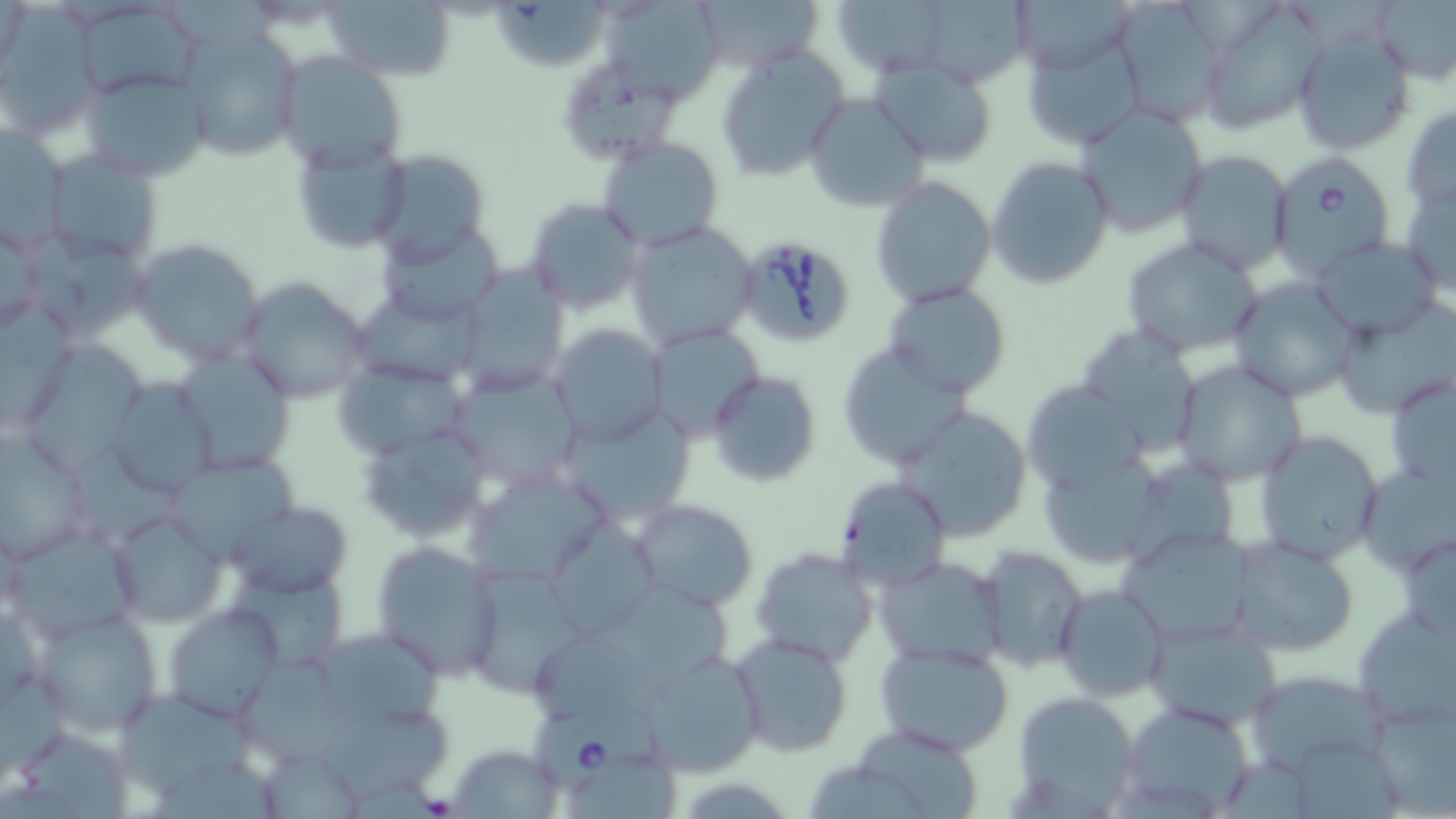

slide-level diagnosis = Babesia divergens
image size = 1456×819 pixels
field of view = one of a larger specimen
uninfected red blood cell locations = approximate bounding boxes as [x1, y1, x2, y2] in pixels: [324, 0, 456, 83], [498, 0, 609, 70], [607, 0, 729, 106], [690, 0, 824, 74], [832, 0, 954, 78], [913, 0, 1031, 88], [1113, 0, 1230, 127], [1200, 0, 1330, 134], [75, 1, 204, 102], [1374, 1, 1456, 85], [1, 8, 102, 140], [178, 27, 303, 163], [1293, 27, 1415, 154], [1020, 30, 1147, 151], [716, 46, 850, 181], [275, 51, 408, 170], [870, 57, 1000, 167], [563, 60, 684, 162], [77, 69, 210, 183], [804, 93, 930, 212], [1400, 105, 1456, 213], [1075, 106, 1210, 237], [2, 121, 69, 254], [596, 135, 725, 252], [290, 140, 411, 255], [40, 147, 164, 267], [368, 150, 491, 266], [1170, 150, 1294, 275], [985, 156, 1115, 290], [870, 176, 995, 306], [1401, 180, 1456, 296], [523, 197, 646, 316], [0, 213, 49, 341], [623, 220, 759, 349], [379, 222, 505, 326], [26, 231, 149, 341], [1122, 235, 1263, 356], [1309, 236, 1442, 341], [130, 237, 265, 368], [454, 264, 572, 392], [237, 276, 374, 406], [1230, 277, 1358, 401], [352, 284, 485, 389], [883, 284, 1012, 400], [0, 300, 75, 431], [1332, 304, 1456, 419], [548, 323, 670, 448], [647, 324, 763, 441], [29, 340, 147, 478], [837, 342, 970, 471], [174, 350, 297, 476], [1172, 360, 1308, 486], [446, 365, 585, 492], [704, 369, 822, 489], [1384, 370, 1455, 490], [105, 376, 218, 498], [1021, 377, 1142, 494], [893, 403, 1036, 540], [556, 404, 699, 525], [358, 418, 493, 544], [0, 426, 97, 566], [1252, 429, 1386, 564], [71, 450, 182, 545], [168, 452, 304, 558], [1358, 465, 1455, 575], [463, 467, 612, 591], [832, 476, 952, 594], [629, 500, 758, 611], [227, 501, 353, 599], [107, 506, 227, 629], [541, 519, 665, 638], [7, 520, 144, 645], [1118, 526, 1255, 644], [1395, 532, 1456, 639], [1226, 534, 1358, 657], [370, 540, 505, 680], [978, 545, 1089, 671], [749, 546, 879, 668], [875, 555, 1007, 665], [230, 564, 354, 673], [465, 566, 591, 698], [590, 578, 737, 691], [1052, 581, 1169, 704], [1353, 601, 1456, 730], [164, 602, 287, 723], [34, 607, 165, 738], [1141, 615, 1286, 732], [728, 631, 853, 756], [322, 633, 447, 727], [871, 638, 1016, 755], [533, 639, 673, 724], [636, 649, 766, 775], [238, 659, 355, 762], [0, 671, 70, 782], [1011, 692, 1139, 811], [119, 695, 252, 795], [1363, 696, 1455, 817], [1117, 697, 1261, 817], [317, 710, 453, 800], [849, 725, 986, 816], [23, 734, 135, 819], [448, 741, 564, 817], [262, 752, 367, 819], [565, 755, 685, 818], [157, 761, 289, 819], [807, 765, 933, 819]
stain = May-Grünwald-Giemsa
preparation = thin blood smear
magnification = 1000x
modality = optical microscopy
Babesia divergens-infected red blood cell locations = approximate bounding boxes as [x1, y1, x2, y2] in pixels: [1270, 150, 1397, 278], [731, 233, 859, 347], [527, 701, 664, 787]